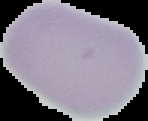

Summary:
  - Image size: 148×121 pixels
  - Image type: segmented cell region with the area outside set to black
  - Preparation: thin blood smear
  - Result: negative for malaria parasites